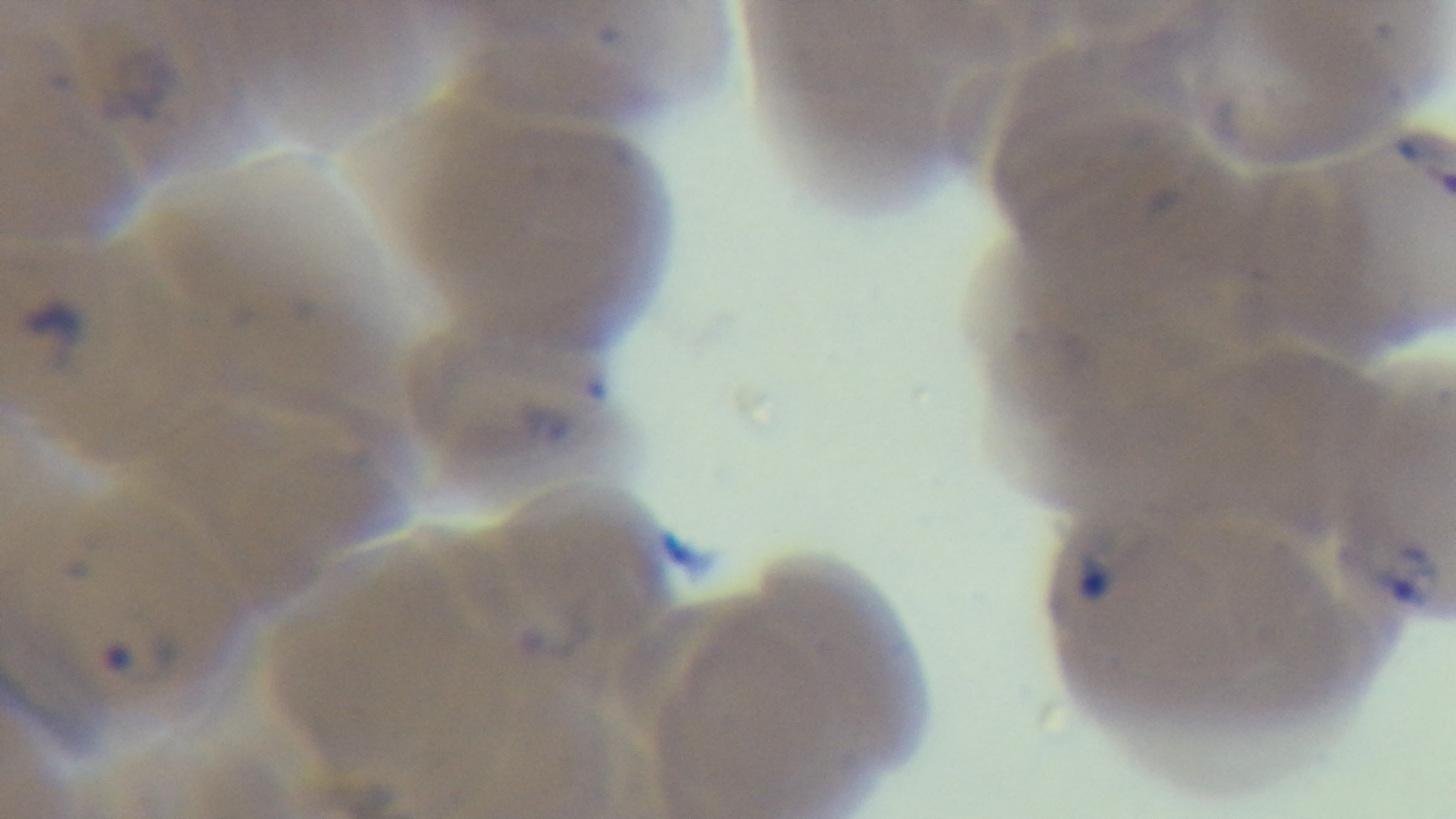

Summary:
  - Preparation: thin smear
  - Capture: mounted 4K digital camera
  - Field of view: single
  - Modality: light microscopy
  - Stain: Giemsa
  - Malaria status: infected
  - Objective: 100x oil immersion